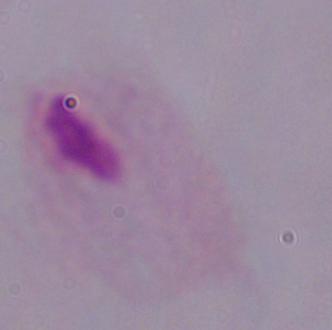

Summary:
  - Modality: photomicrograph
  - Identification: trichomonad
  - Magnification: 1000x